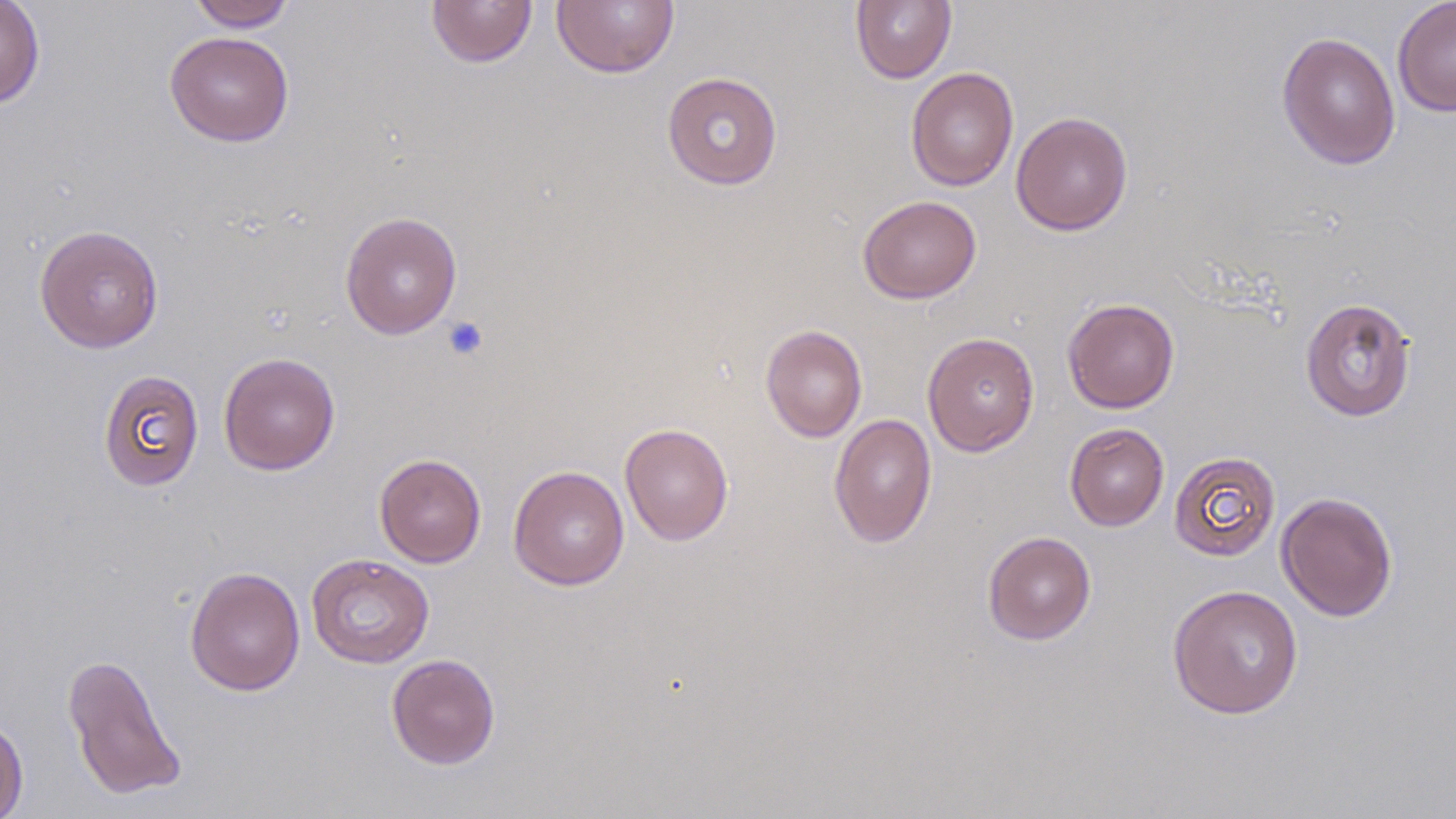

Summary:
  - Coordinate format: approximate bounding boxes as named x1/y1/x2/y2 corners in pixels
  - Platelet locations: (x1=441, y1=316, x2=489, y2=361)
  - Uninfected red blood cell locations: (x1=188, y1=0, x2=297, y2=31), (x1=426, y1=0, x2=538, y2=68), (x1=552, y1=0, x2=680, y2=79), (x1=850, y1=0, x2=957, y2=84), (x1=1392, y1=0, x2=1456, y2=117), (x1=0, y1=1, x2=45, y2=108), (x1=164, y1=31, x2=295, y2=147), (x1=1276, y1=31, x2=1401, y2=170), (x1=905, y1=67, x2=1019, y2=191), (x1=662, y1=71, x2=783, y2=190), (x1=1010, y1=111, x2=1133, y2=236), (x1=857, y1=195, x2=982, y2=304), (x1=340, y1=211, x2=463, y2=339), (x1=34, y1=224, x2=164, y2=353), (x1=1062, y1=297, x2=1180, y2=413), (x1=1299, y1=297, x2=1417, y2=422), (x1=760, y1=324, x2=867, y2=443), (x1=922, y1=331, x2=1040, y2=456), (x1=219, y1=352, x2=340, y2=475), (x1=98, y1=368, x2=204, y2=491), (x1=828, y1=413, x2=938, y2=549), (x1=620, y1=423, x2=734, y2=546), (x1=1065, y1=423, x2=1169, y2=531), (x1=1168, y1=450, x2=1281, y2=562), (x1=374, y1=453, x2=486, y2=568), (x1=508, y1=465, x2=630, y2=591), (x1=1276, y1=491, x2=1398, y2=622), (x1=982, y1=530, x2=1096, y2=645), (x1=306, y1=553, x2=435, y2=668), (x1=185, y1=565, x2=305, y2=696), (x1=1167, y1=584, x2=1304, y2=720), (x1=63, y1=653, x2=187, y2=801), (x1=386, y1=653, x2=501, y2=770), (x1=0, y1=715, x2=28, y2=819)
  - Slide-level diagnosis: negative for blood parasites
  - Stain: May-Grünwald-Giemsa
  - Preparation: thin blood film
  - Field of view: one of a larger specimen
  - Image size: 1456×819 pixels
  - Magnification: 1000x
  - Modality: light microscopy